Classify this cell by malaria status.
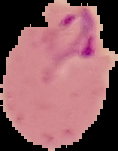

Parasitized.

Cell region segmented out of the field of view; the surrounding area is masked to black. Image is 118×151 pixels. From a thin blood smear.